Locate every uninfected red blood cell.
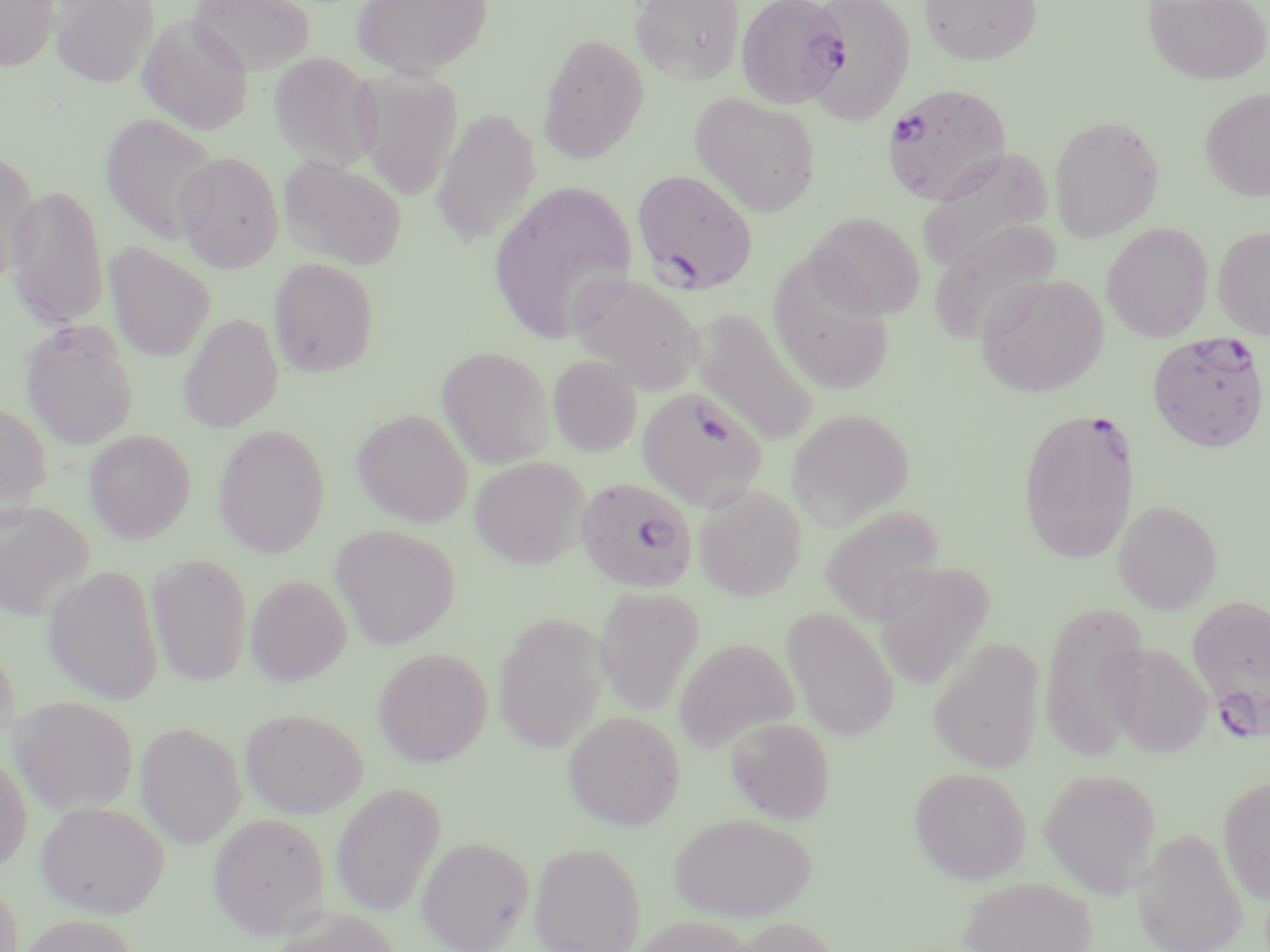
Approximate bounding boxes as named x1/y1/x2/y2 corners in pixels.
Uninfected red blood cells: (x1=0, y1=0, x2=60, y2=71), (x1=51, y1=0, x2=159, y2=87), (x1=188, y1=0, x2=315, y2=75), (x1=351, y1=0, x2=493, y2=79), (x1=630, y1=0, x2=744, y2=85), (x1=805, y1=0, x2=915, y2=125), (x1=919, y1=0, x2=1043, y2=65), (x1=1143, y1=0, x2=1270, y2=85), (x1=137, y1=14, x2=253, y2=135), (x1=537, y1=33, x2=649, y2=164), (x1=269, y1=52, x2=381, y2=174), (x1=353, y1=68, x2=464, y2=201), (x1=1200, y1=87, x2=1270, y2=202), (x1=690, y1=92, x2=822, y2=217), (x1=432, y1=108, x2=542, y2=248), (x1=100, y1=112, x2=220, y2=244), (x1=1049, y1=115, x2=1165, y2=242), (x1=0, y1=147, x2=41, y2=283), (x1=917, y1=148, x2=1055, y2=274), (x1=174, y1=151, x2=284, y2=272), (x1=277, y1=155, x2=407, y2=270), (x1=488, y1=180, x2=639, y2=344), (x1=6, y1=184, x2=110, y2=331), (x1=807, y1=212, x2=925, y2=319), (x1=1101, y1=223, x2=1214, y2=343), (x1=1212, y1=226, x2=1270, y2=339), (x1=104, y1=242, x2=215, y2=362), (x1=767, y1=255, x2=896, y2=396), (x1=268, y1=258, x2=379, y2=378), (x1=569, y1=271, x2=704, y2=393), (x1=975, y1=274, x2=1109, y2=398), (x1=690, y1=308, x2=820, y2=447), (x1=179, y1=313, x2=283, y2=434), (x1=20, y1=321, x2=138, y2=450), (x1=436, y1=346, x2=555, y2=469), (x1=548, y1=355, x2=642, y2=456), (x1=0, y1=399, x2=52, y2=526), (x1=352, y1=408, x2=473, y2=528), (x1=786, y1=408, x2=914, y2=531), (x1=213, y1=424, x2=330, y2=558), (x1=84, y1=430, x2=195, y2=544), (x1=469, y1=455, x2=590, y2=569), (x1=693, y1=483, x2=807, y2=601), (x1=1113, y1=500, x2=1223, y2=614), (x1=0, y1=501, x2=94, y2=621), (x1=819, y1=505, x2=945, y2=627), (x1=330, y1=525, x2=460, y2=650), (x1=147, y1=552, x2=253, y2=687), (x1=874, y1=561, x2=996, y2=689), (x1=44, y1=565, x2=163, y2=705), (x1=245, y1=575, x2=351, y2=686), (x1=594, y1=585, x2=704, y2=716), (x1=781, y1=606, x2=899, y2=741), (x1=494, y1=612, x2=609, y2=753), (x1=0, y1=634, x2=20, y2=749), (x1=928, y1=637, x2=1045, y2=774), (x1=674, y1=639, x2=799, y2=752), (x1=1102, y1=642, x2=1215, y2=758), (x1=372, y1=647, x2=492, y2=767), (x1=9, y1=696, x2=139, y2=815), (x1=240, y1=707, x2=369, y2=818), (x1=563, y1=710, x2=686, y2=831), (x1=726, y1=716, x2=835, y2=824), (x1=135, y1=721, x2=247, y2=848), (x1=0, y1=751, x2=32, y2=874), (x1=909, y1=766, x2=1031, y2=885), (x1=1039, y1=768, x2=1161, y2=897), (x1=1218, y1=774, x2=1270, y2=904), (x1=330, y1=782, x2=446, y2=917), (x1=35, y1=800, x2=170, y2=918), (x1=208, y1=812, x2=330, y2=939), (x1=668, y1=812, x2=817, y2=922), (x1=1134, y1=827, x2=1248, y2=952), (x1=416, y1=835, x2=533, y2=951), (x1=529, y1=841, x2=646, y2=952), (x1=959, y1=876, x2=1097, y2=952), (x1=0, y1=878, x2=25, y2=952), (x1=271, y1=907, x2=401, y2=952), (x1=15, y1=914, x2=142, y2=952), (x1=630, y1=915, x2=758, y2=952), (x1=725, y1=917, x2=842, y2=952).

Plasmodium falciparum-infected red blood cell locations: (x1=736, y1=0, x2=850, y2=109), (x1=883, y1=84, x2=1012, y2=206), (x1=632, y1=169, x2=757, y2=295), (x1=1147, y1=330, x2=1268, y2=452), (x1=636, y1=385, x2=767, y2=511), (x1=1017, y1=406, x2=1138, y2=564), (x1=576, y1=478, x2=698, y2=594), (x1=1187, y1=593, x2=1270, y2=739). Slide-level diagnosis: Plasmodium falciparum. Single field of view. May-Grünwald-Giemsa stain. 1000x magnification. Light microscopy. Image is 1270×952 pixels. Thin blood film.